Identify the parasite.
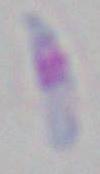

Toxoplasma gondii.

Summary:
  - Modality: photomicrograph
  - Magnification: 1000x